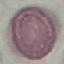
result = no malaria parasites detected
preparation = thin blood film
stain = Giemsa
capture = smartphone through the microscope eyepiece
image type = cell patch, automatically extracted from a larger field of view and resized to 64 × 64 pixels